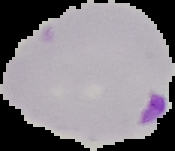
From a thin blood smear. Image is 175×151 pixels. Malaria status: parasitized. Cell region segmented out of the field of view; the surrounding area is masked to black.